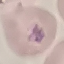

malaria status = parasitized
stain = Giemsa
capture = smartphone through the microscope eyepiece
image type = automatically extracted cell patch, resized to 64 × 64 pixels
preparation = thin blood smear